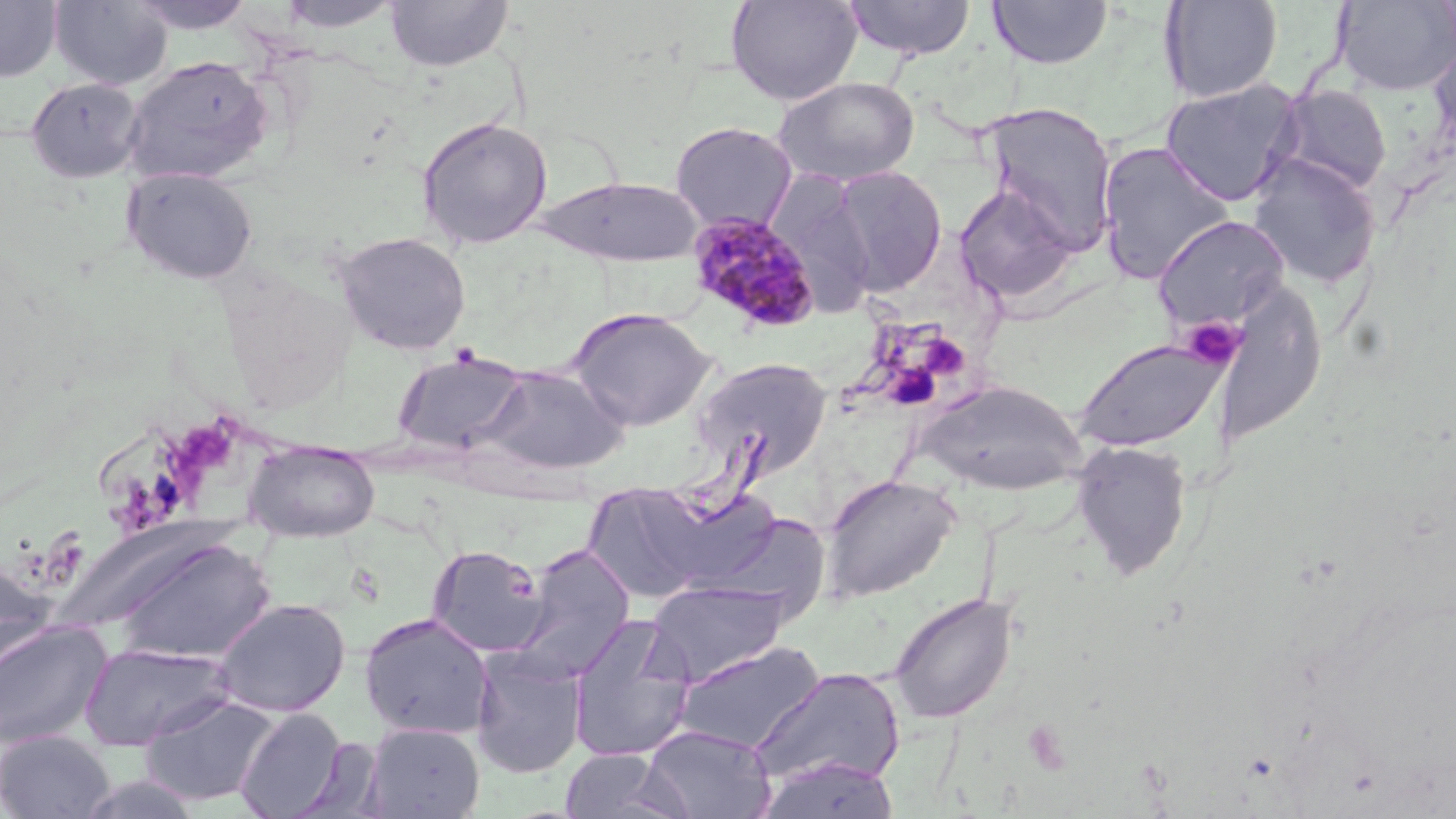

Summary:
  - Coordinate format: approximate bounding boxes as named x1/y1/x2/y2 corners in pixels
  - Platelet locations: (x1=1182, y1=317, x2=1246, y2=370), (x1=918, y1=333, x2=970, y2=381), (x1=1023, y1=719, x2=1075, y2=776)
  - Plasmodium malariae-infected red blood cell locations: (x1=687, y1=212, x2=821, y2=335)
  - Uninfected red blood cell locations: (x1=0, y1=0, x2=62, y2=82), (x1=51, y1=0, x2=173, y2=91), (x1=127, y1=0, x2=259, y2=34), (x1=277, y1=0, x2=402, y2=32), (x1=385, y1=0, x2=512, y2=72), (x1=725, y1=0, x2=863, y2=105), (x1=840, y1=0, x2=977, y2=60), (x1=987, y1=0, x2=1113, y2=69), (x1=1159, y1=0, x2=1284, y2=103), (x1=1333, y1=1, x2=1456, y2=95), (x1=1428, y1=37, x2=1456, y2=157), (x1=122, y1=55, x2=272, y2=184), (x1=775, y1=76, x2=920, y2=185), (x1=27, y1=78, x2=144, y2=183), (x1=1159, y1=78, x2=1304, y2=206), (x1=1273, y1=85, x2=1392, y2=196), (x1=982, y1=102, x2=1118, y2=253), (x1=417, y1=116, x2=552, y2=249), (x1=670, y1=121, x2=797, y2=233), (x1=1096, y1=141, x2=1234, y2=284), (x1=1247, y1=154, x2=1382, y2=288), (x1=830, y1=166, x2=948, y2=294), (x1=122, y1=167, x2=258, y2=284), (x1=768, y1=173, x2=876, y2=314), (x1=537, y1=176, x2=703, y2=266), (x1=953, y1=183, x2=1077, y2=304), (x1=1152, y1=215, x2=1290, y2=333), (x1=335, y1=231, x2=471, y2=354), (x1=568, y1=307, x2=716, y2=431), (x1=1074, y1=338, x2=1229, y2=453), (x1=393, y1=351, x2=529, y2=455), (x1=693, y1=357, x2=833, y2=479), (x1=481, y1=366, x2=630, y2=475), (x1=916, y1=380, x2=1086, y2=494), (x1=243, y1=439, x2=380, y2=541), (x1=1071, y1=440, x2=1193, y2=582), (x1=821, y1=474, x2=959, y2=602), (x1=584, y1=486, x2=716, y2=602), (x1=650, y1=487, x2=787, y2=592), (x1=705, y1=509, x2=832, y2=620), (x1=109, y1=539, x2=276, y2=665), (x1=427, y1=545, x2=549, y2=657), (x1=508, y1=545, x2=636, y2=683), (x1=0, y1=559, x2=57, y2=682), (x1=646, y1=578, x2=791, y2=686), (x1=888, y1=590, x2=1018, y2=724), (x1=212, y1=598, x2=351, y2=717), (x1=359, y1=611, x2=494, y2=740), (x1=567, y1=613, x2=697, y2=762), (x1=0, y1=620, x2=113, y2=749), (x1=674, y1=640, x2=825, y2=754), (x1=79, y1=642, x2=237, y2=751), (x1=470, y1=647, x2=587, y2=779), (x1=748, y1=668, x2=906, y2=791), (x1=139, y1=694, x2=280, y2=807), (x1=235, y1=708, x2=346, y2=818), (x1=363, y1=722, x2=484, y2=818), (x1=643, y1=724, x2=776, y2=819), (x1=0, y1=730, x2=115, y2=819), (x1=291, y1=737, x2=386, y2=819), (x1=558, y1=748, x2=688, y2=819), (x1=754, y1=755, x2=901, y2=818), (x1=77, y1=773, x2=202, y2=818)
  - Slide-level diagnosis: Plasmodium malariae
  - Preparation: thin blood smear
  - Field of view: one of a larger specimen
  - Image size: 1456×819 pixels
  - Modality: optical microscopy
  - Magnification: 1000x
  - Stain: May-Grünwald-Giemsa